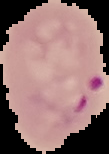
Summary:
  - Image type: segmented cell region on a black background
  - Preparation: thin blood smear
  - Image size: 109×154 pixels
  - Result: Plasmodium parasites detected